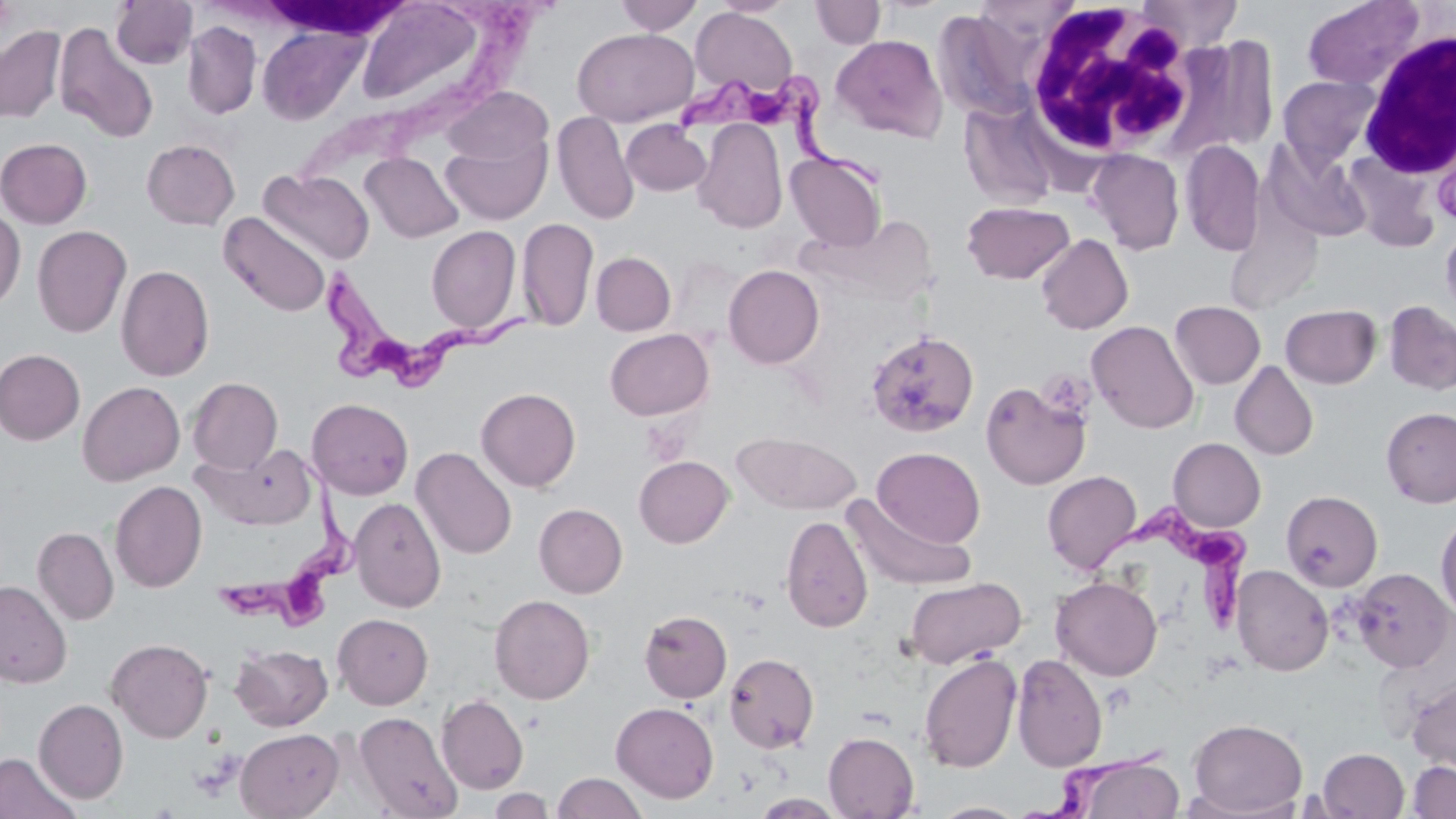

Approximate bounding boxes as (x1, y1, x2, y2) in pixels. Uninfected red blood cell locations: (354, 0, 492, 113), (615, 0, 703, 34), (714, 0, 795, 17), (810, 0, 885, 49), (1138, 0, 1243, 50), (1302, 0, 1426, 91), (111, 1, 197, 70), (691, 7, 797, 96), (183, 21, 261, 119), (54, 22, 160, 144), (257, 23, 368, 125), (0, 26, 66, 124), (572, 28, 697, 127), (830, 34, 948, 142), (1277, 75, 1382, 171), (443, 87, 552, 166), (962, 104, 1059, 211), (552, 112, 638, 225), (693, 119, 787, 233), (621, 120, 713, 196), (440, 131, 551, 225), (0, 138, 93, 228), (142, 139, 240, 230), (1180, 140, 1265, 256), (1264, 141, 1372, 243), (1088, 149, 1184, 255), (361, 152, 463, 243), (786, 152, 887, 252), (259, 169, 374, 265), (961, 201, 1074, 284), (0, 207, 26, 312), (219, 212, 332, 317), (517, 217, 599, 333), (1440, 223, 1456, 322), (32, 225, 131, 338), (426, 226, 521, 334), (1036, 234, 1133, 335), (591, 252, 676, 335), (116, 264, 214, 382), (723, 265, 824, 368), (1170, 300, 1265, 389), (1384, 301, 1456, 395), (1280, 304, 1382, 388), (1086, 320, 1199, 434), (605, 328, 713, 420), (866, 330, 979, 438), (0, 349, 85, 445), (1230, 361, 1318, 461), (187, 377, 283, 473), (980, 380, 1090, 490), (78, 381, 185, 485), (476, 387, 581, 492), (307, 398, 413, 500), (1381, 407, 1456, 508), (732, 432, 861, 514), (1168, 438, 1266, 532), (193, 442, 316, 530), (873, 446, 985, 548), (412, 447, 517, 560), (634, 455, 734, 547), (1042, 471, 1141, 574), (110, 480, 207, 592), (1280, 489, 1383, 591), (844, 496, 976, 591), (350, 497, 446, 612), (534, 503, 628, 598), (1435, 512, 1456, 621), (780, 514, 873, 633), (33, 527, 119, 624), (1231, 565, 1333, 676), (1351, 568, 1455, 672), (905, 576, 1026, 668), (1051, 576, 1162, 680), (0, 580, 72, 688), (489, 594, 595, 704), (639, 609, 732, 703), (333, 613, 433, 709), (107, 637, 213, 743), (230, 643, 333, 731), (724, 653, 819, 753), (918, 653, 1022, 773), (1011, 653, 1108, 771), (1407, 676, 1456, 776), (436, 694, 529, 794), (34, 698, 129, 803), (611, 701, 719, 803), (354, 711, 462, 819), (1188, 718, 1308, 815), (235, 728, 344, 818), (823, 731, 919, 818), (1317, 748, 1409, 818), (0, 752, 81, 819), (1073, 756, 1184, 819), (1407, 760, 1456, 818), (552, 772, 647, 818), (488, 788, 556, 818), (751, 793, 845, 817), (930, 801, 1027, 818). Trypanosoma brucei locations: (678, 74, 889, 194), (312, 263, 534, 388), (210, 439, 362, 640), (1077, 501, 1255, 633), (1032, 738, 1172, 818). White blood cell locations: (1021, 4, 1201, 163), (1355, 28, 1455, 179). Slide-level diagnosis: Trypanosoma brucei. Single field of view. Captured at 1000x magnification. May-Grünwald-Giemsa-stained preparation. Thin blood film. Optical microscopy. Image is 1456×819 pixels.